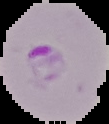

Result: malaria parasites detected. Image is 109×124 pixels. From a thin blood smear. The area outside the segmented cell region is set to black.